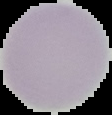
preparation: thin blood film
image_type: segmented cell region on a black background
result: no malaria parasites detected
image_size: 112×115 pixels